Outline each blood parasite and name the species.
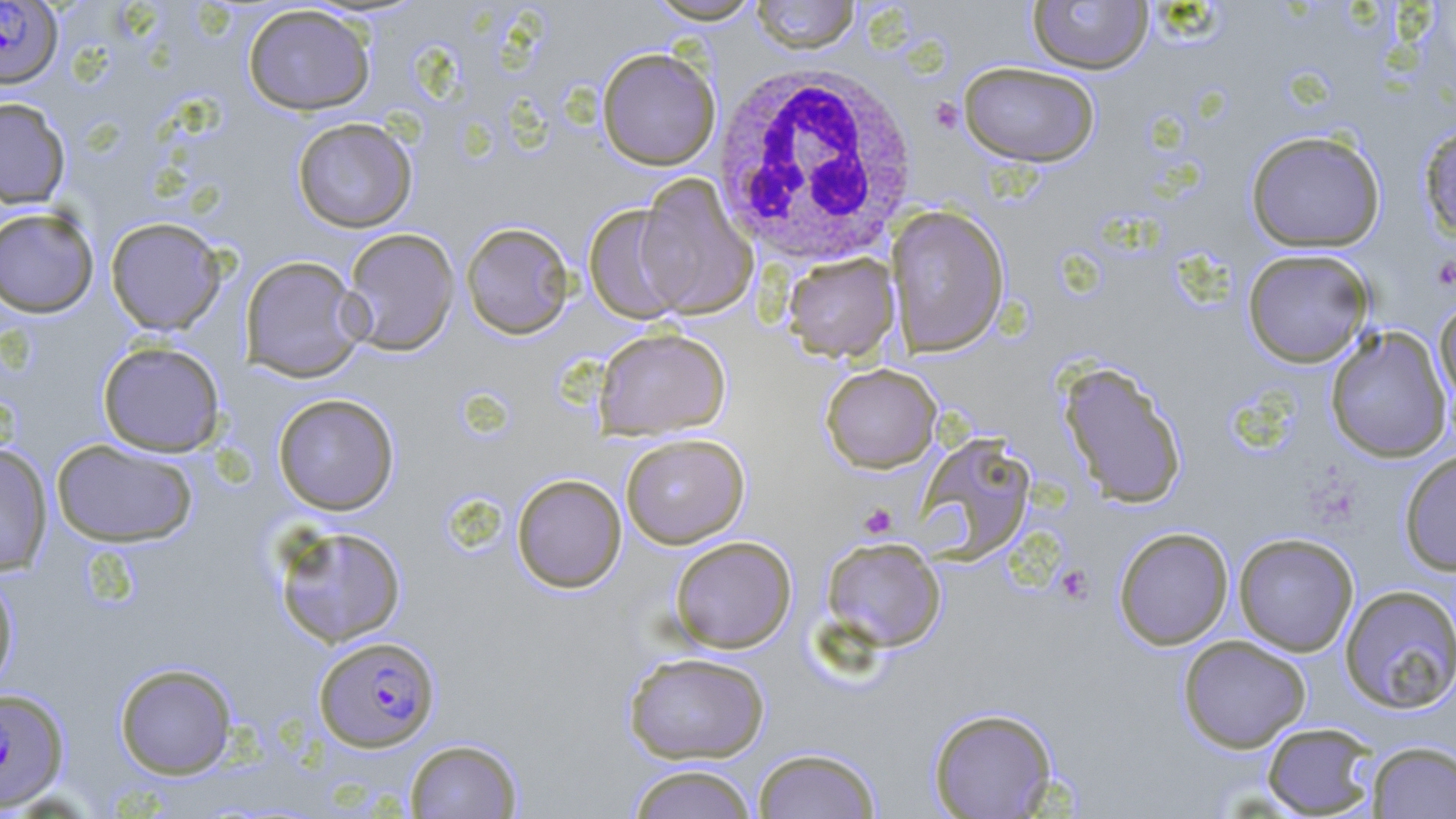
Approximate bounding boxes as [x1, y1, x2, y2] in pixels.
Plasmodium falciparum-infected red blood cells: [0, 1, 63, 89], [314, 635, 440, 751], [0, 687, 69, 811].
No Plasmodium ovale, Plasmodium malariae, Plasmodium vivax, Babesia divergens, or Trypanosoma brucei observed.

Uninfected red blood cell locations: [645, 0, 764, 24], [749, 0, 860, 54], [1027, 0, 1154, 74], [242, 4, 375, 116], [596, 47, 721, 170], [959, 61, 1101, 167], [0, 96, 71, 208], [291, 117, 418, 233], [1418, 122, 1456, 243], [1245, 130, 1386, 253], [633, 175, 758, 320], [583, 204, 688, 324], [886, 204, 1010, 357], [0, 206, 100, 318], [105, 217, 228, 335], [461, 221, 575, 339], [341, 227, 460, 356], [1242, 249, 1374, 367], [782, 252, 900, 362], [239, 255, 367, 382], [1434, 299, 1456, 415], [1324, 325, 1453, 463], [594, 327, 732, 439], [97, 341, 226, 456], [1057, 361, 1188, 509], [820, 363, 942, 473], [273, 393, 399, 515], [620, 433, 750, 548], [915, 434, 1037, 563], [50, 437, 199, 548], [0, 443, 53, 576], [1399, 449, 1456, 576], [511, 473, 627, 593], [272, 524, 407, 648], [1113, 526, 1233, 650], [1233, 532, 1359, 656], [669, 535, 797, 653], [821, 537, 947, 652], [0, 569, 19, 693], [1339, 584, 1455, 715], [1178, 635, 1311, 752], [623, 651, 771, 764], [114, 662, 238, 779], [927, 706, 1058, 818], [1261, 721, 1379, 817], [404, 738, 523, 818], [1367, 741, 1456, 818], [753, 747, 882, 819], [626, 764, 759, 819]. White blood cell locations: [711, 62, 921, 267]. Platelet locations: [1432, 255, 1456, 292], [857, 502, 898, 539], [1056, 564, 1094, 605]. Slide-level diagnosis: Plasmodium falciparum. Captured at 1000x magnification. May-Grünwald-Giemsa stain. Thin blood smear. Image is 1456×819 pixels. Optical microscopy. Single field of view.